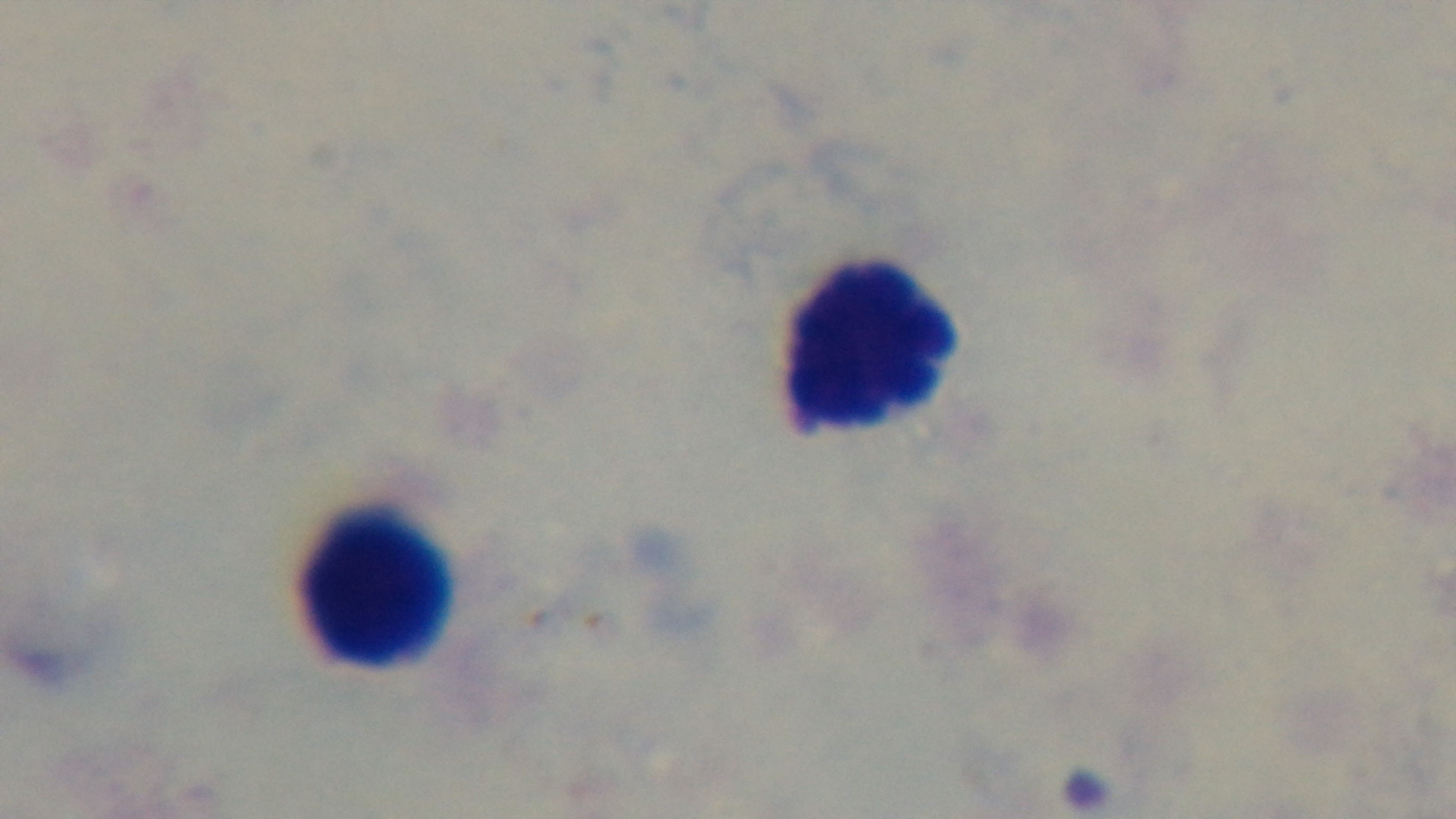

Giemsa-stained. Preparation: thick. Single field of view. Photomicrograph. Mounted 4K digital camera. Malaria status: negative. Oil-immersion objective, 100x.